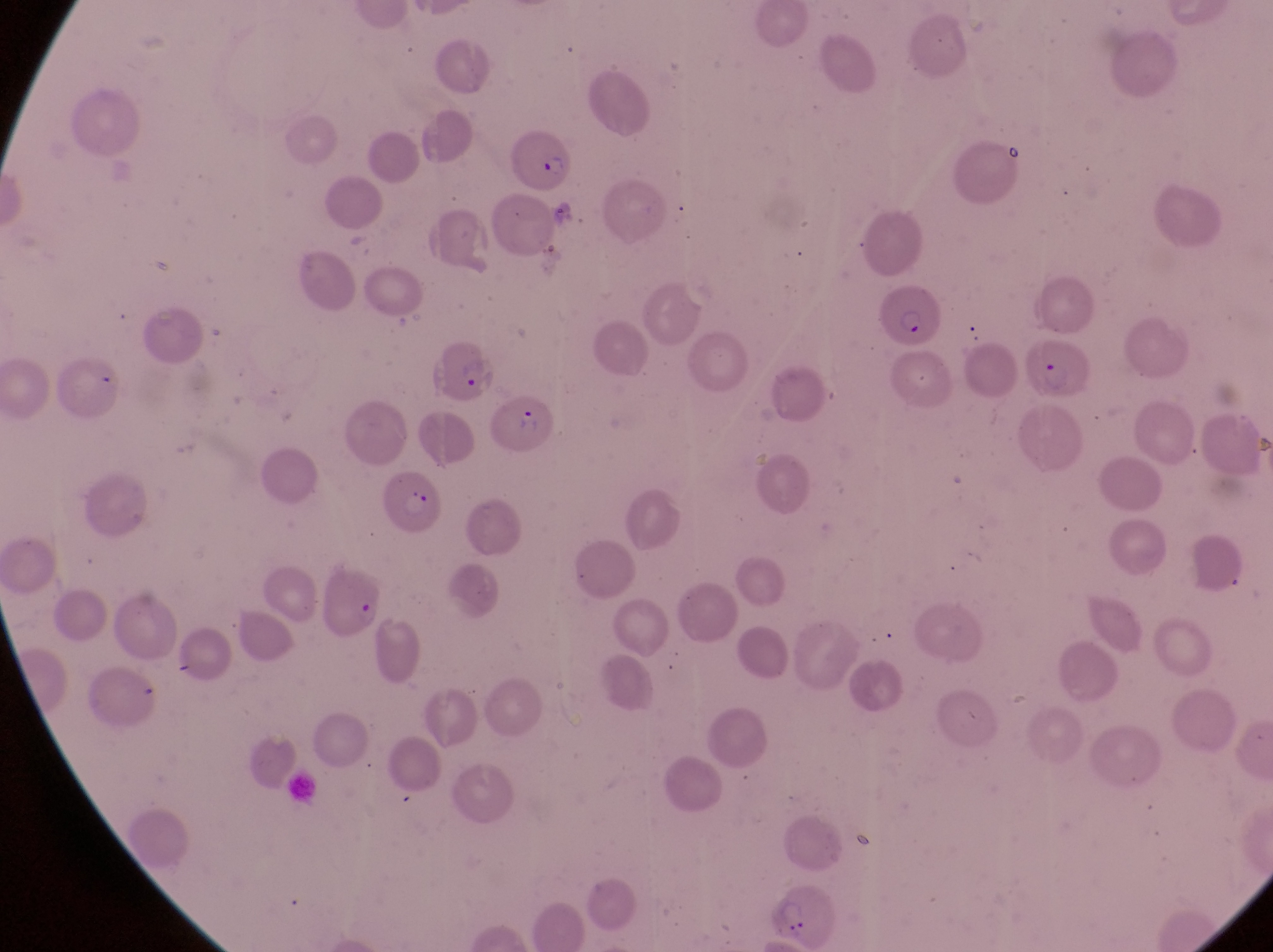

country = Uganda
parasitised red blood cell locations = approximate bounding boxes as {left, top, right, bottom} in pixels: {500, 123, 572, 197}, {876, 289, 941, 352}, {1026, 334, 1095, 404}, {424, 337, 494, 402}, {484, 390, 558, 458}, {382, 465, 449, 535}, {324, 564, 387, 647}
preparation = thin blood smear
image size = 1273×952 pixels
field of view = single
magnification = 1000x
capture = smartphone photograph through the eyepiece of an Olympus CX-23 microscope